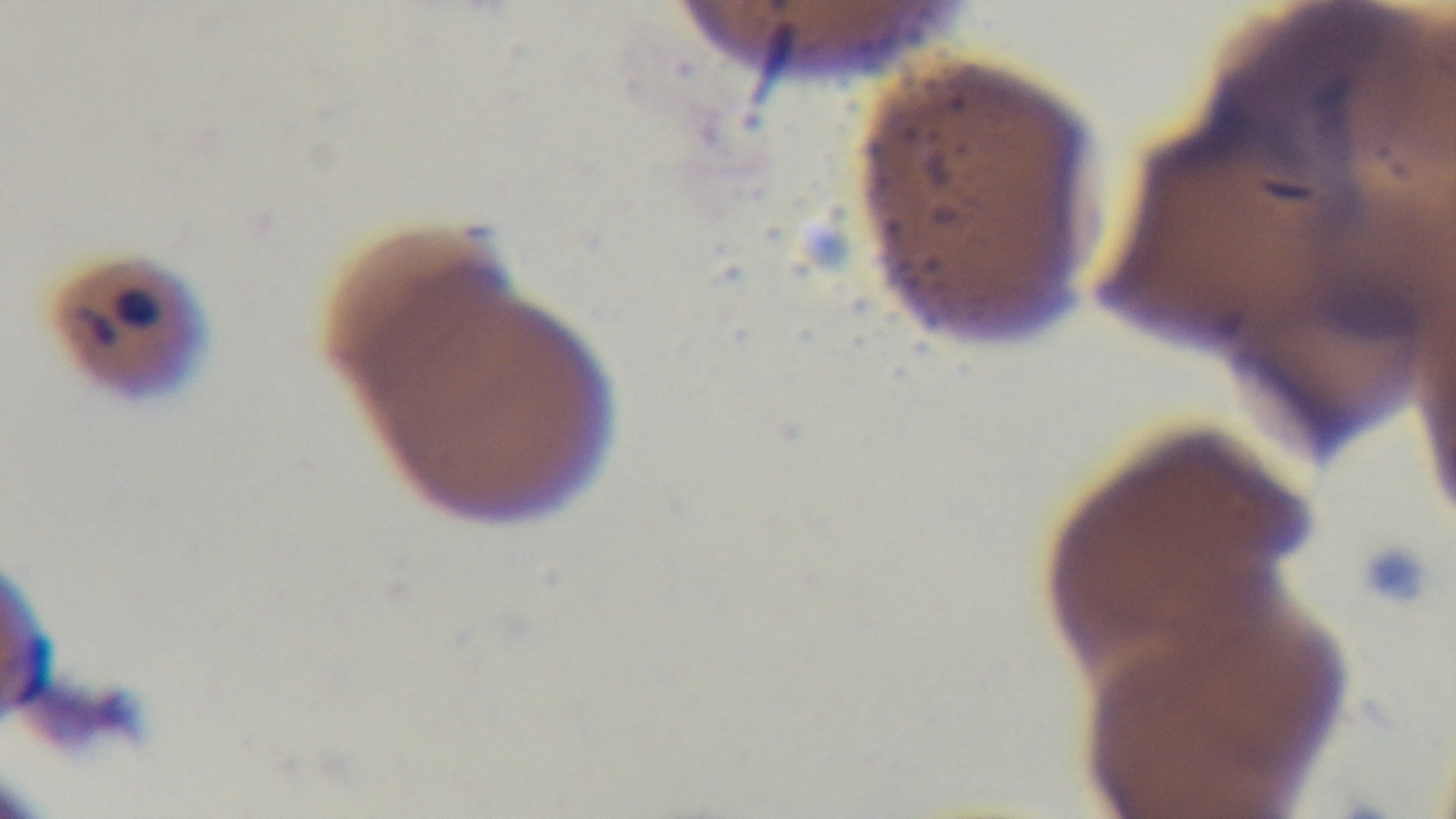
One field from the slide. Malaria status: infected. Giemsa stain. Light microscopy. Preparation: thin smear. Mounted 4K digital camera. 100x oil-immersion objective.